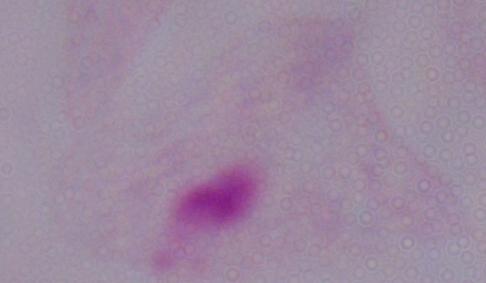

{
  "magnification": "1000x",
  "modality": "photomicrograph",
  "identification": "trichomonad"
}